Comment on the background quality.
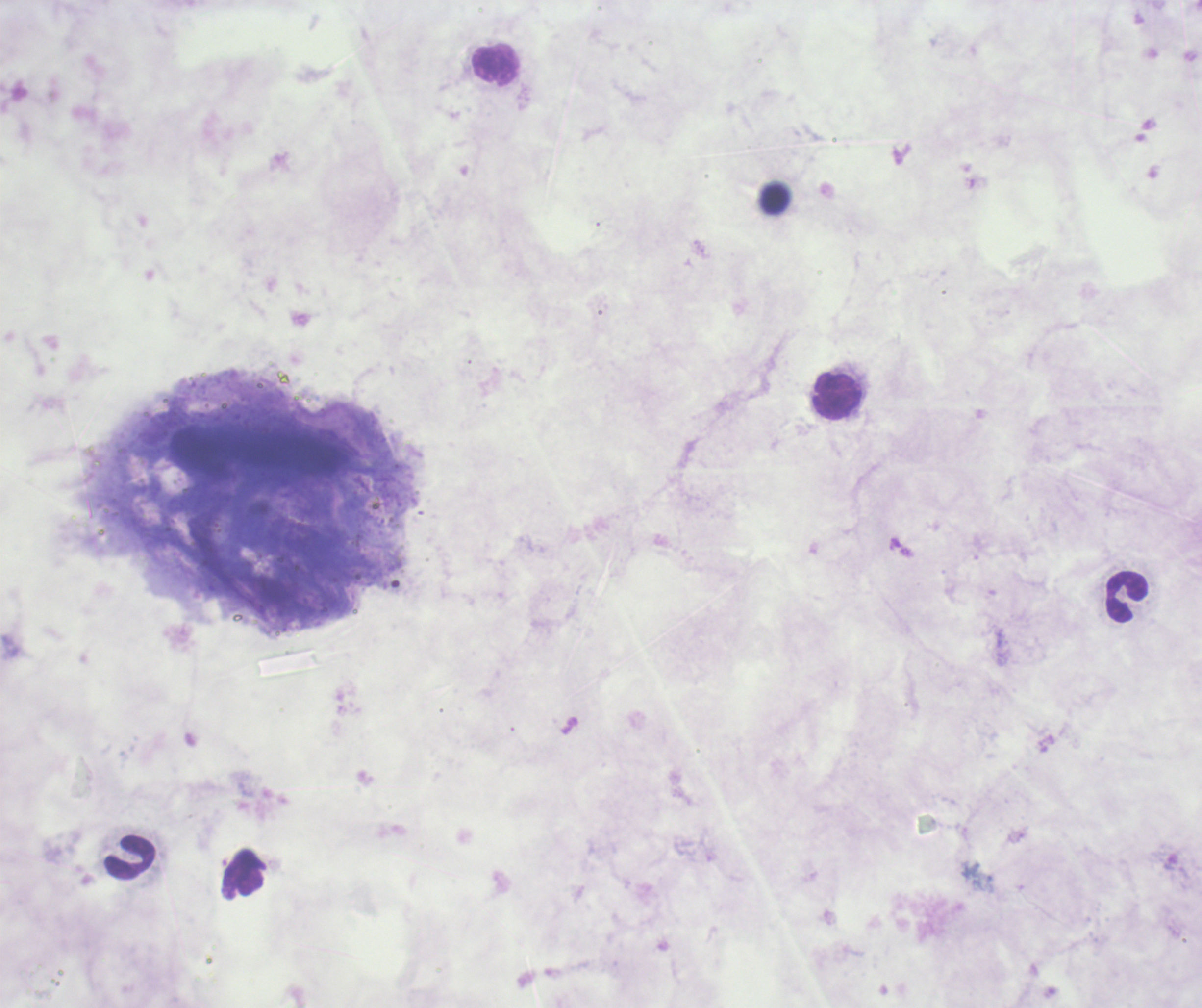
Poor.

coordinate format = approximate object centers, in pixels from the top-left corner
leukocyte locations = (x=496, y=65), (x=775, y=199), (x=837, y=396), (x=1126, y=597), (x=130, y=856), (x=243, y=873)
coloration quality = bad
stain = Romanowsky
result = negative for malaria parasites
field of view = one from this slide
context = previously used in a real diagnosis
preparation = thick blood film
image size = 1202×1008 pixels
magnification = 100x